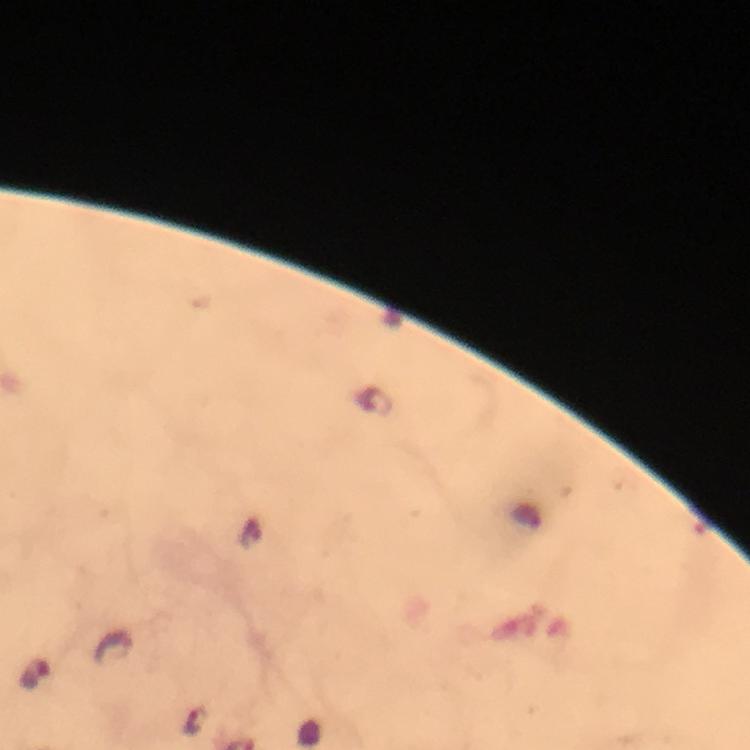
Approximate object centers, in pixels from the top-left corner. Malaria parasite locations: (x=35, y=677), (x=196, y=720). A crop from one field of view. Giemsa stain. Thick smear. From a malaria diagnostic workup. Immersion oil was used. Photographed through the microscope with a smartphone camera. Image is 750×750 pixels. At 100x magnification.